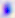
Captured at 400x magnification. Toxoplasma gondii is seen. Photomicrograph.